Assess this cell for malaria.
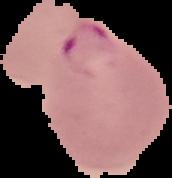
Parasitized.

Cell region segmented out of the field of view; the surrounding area is masked to black. Image is 172×178 pixels. From a thin blood smear.